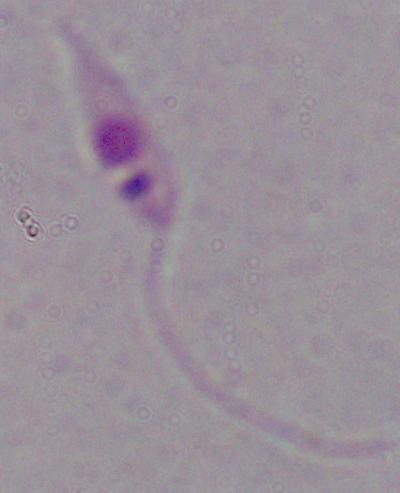

Summary:
  - Modality: micrograph
  - Magnification: 1000x
  - Identification: Leishmania